Comment on the morphology of the erythrocytes.
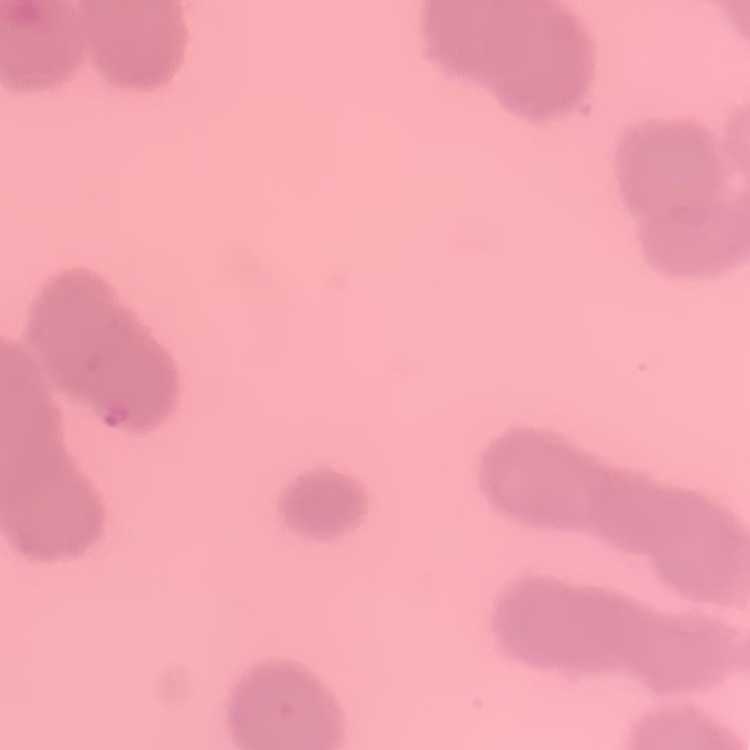

Rouleaux formation.

Square crop of a larger photomicrograph. Thin blood film. Field's or Giemsa stain.